Assess this cell for malaria.
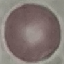

Uninfected.

stain: Giemsa
image_type: cell patch, automatically extracted from a larger field of view and resized to 64 × 64 pixels
preparation: thin smear
capture: smartphone camera at the microscope eyepiece